Assess the morphology of the erythrocytes.
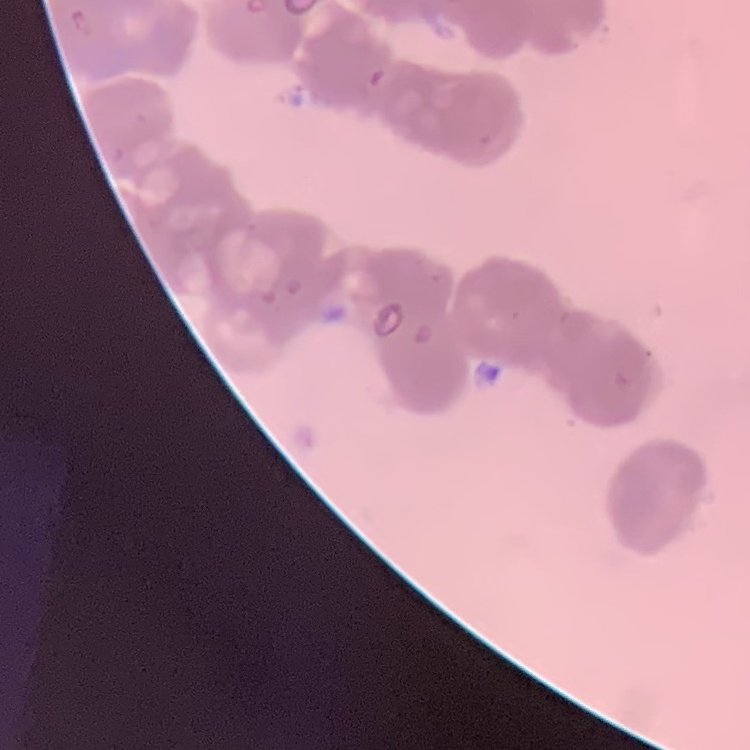
They show rouleaux formation.

Stained with either Field's or Giemsa. Square crop of a larger photomicrograph. Thin peripheral smear.